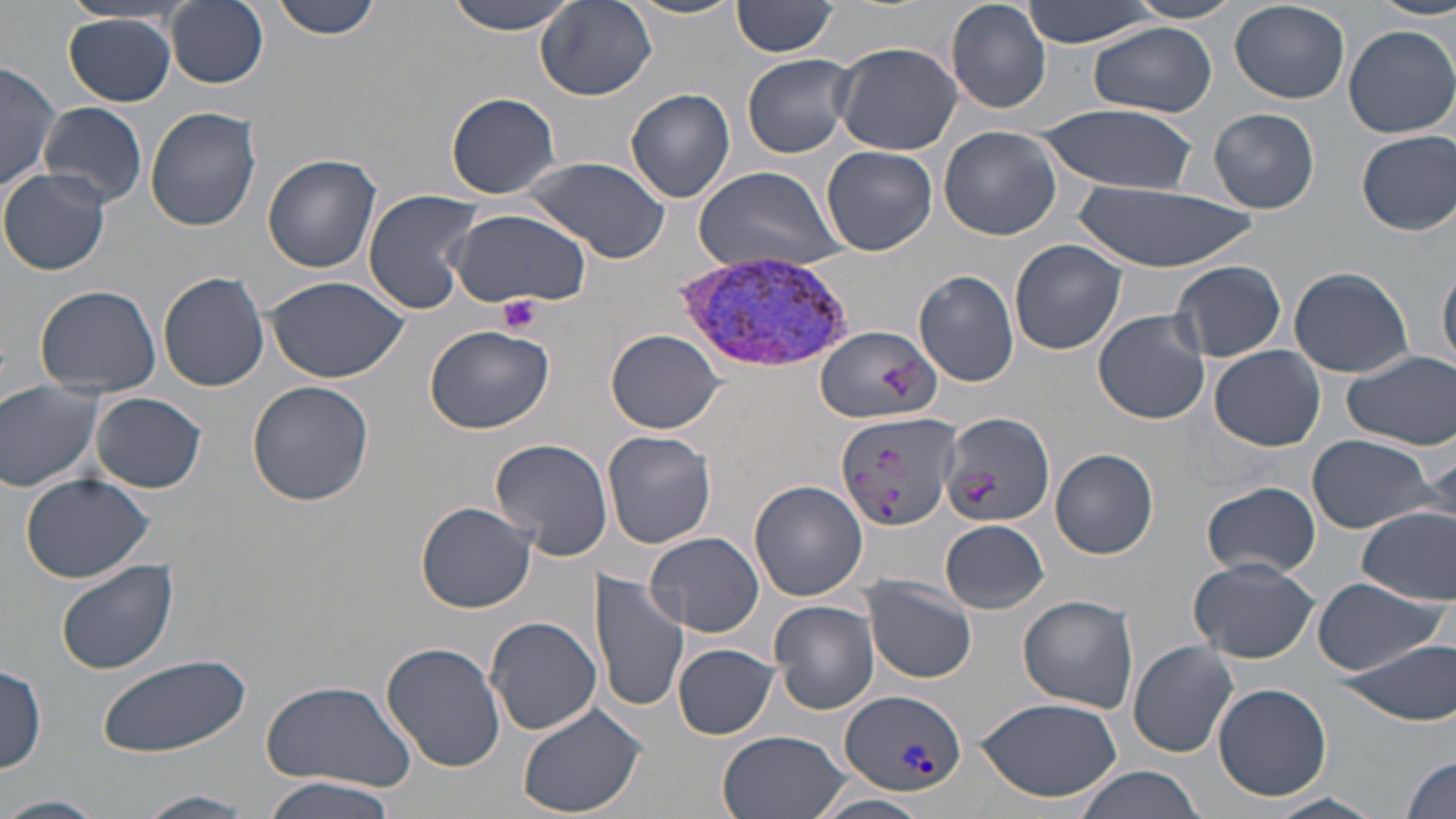

Summary:
  - Coordinate format: approximate bounding boxes as named x1/y1/x2/y2 corners in pixels
  - Platelet locations: (x1=500, y1=294, x2=540, y2=334)
  - Plasmodium vivax-infected red blood cell locations: (x1=677, y1=249, x2=853, y2=374), (x1=839, y1=689, x2=965, y2=797)
  - Uninfected red blood cell locations: (x1=165, y1=0, x2=270, y2=88), (x1=271, y1=0, x2=382, y2=40), (x1=442, y1=0, x2=584, y2=34), (x1=535, y1=0, x2=658, y2=101), (x1=624, y1=0, x2=747, y2=20), (x1=946, y1=0, x2=1052, y2=115), (x1=1019, y1=0, x2=1162, y2=48), (x1=1124, y1=0, x2=1246, y2=22), (x1=733, y1=1, x2=840, y2=57), (x1=1373, y1=1, x2=1456, y2=21), (x1=1229, y1=2, x2=1351, y2=104), (x1=65, y1=14, x2=179, y2=106), (x1=1087, y1=23, x2=1216, y2=117), (x1=1344, y1=25, x2=1456, y2=138), (x1=835, y1=40, x2=966, y2=156), (x1=742, y1=53, x2=856, y2=159), (x1=0, y1=59, x2=60, y2=192), (x1=626, y1=88, x2=736, y2=204), (x1=446, y1=92, x2=560, y2=198), (x1=39, y1=103, x2=147, y2=208), (x1=1034, y1=104, x2=1198, y2=193), (x1=146, y1=106, x2=261, y2=231), (x1=1210, y1=108, x2=1319, y2=214), (x1=939, y1=125, x2=1063, y2=241), (x1=1357, y1=130, x2=1456, y2=235), (x1=821, y1=145, x2=938, y2=256), (x1=263, y1=154, x2=381, y2=272), (x1=520, y1=155, x2=673, y2=265), (x1=688, y1=163, x2=849, y2=273), (x1=0, y1=170, x2=111, y2=275), (x1=1071, y1=183, x2=1257, y2=271), (x1=362, y1=189, x2=482, y2=315), (x1=446, y1=205, x2=591, y2=309), (x1=1009, y1=240, x2=1127, y2=355), (x1=1172, y1=260, x2=1287, y2=361), (x1=1439, y1=264, x2=1456, y2=372), (x1=1289, y1=266, x2=1413, y2=378), (x1=913, y1=270, x2=1021, y2=387), (x1=157, y1=271, x2=269, y2=392), (x1=268, y1=275, x2=407, y2=382), (x1=34, y1=284, x2=162, y2=397), (x1=1093, y1=309, x2=1212, y2=424), (x1=424, y1=324, x2=554, y2=434), (x1=816, y1=327, x2=941, y2=428), (x1=607, y1=329, x2=725, y2=432), (x1=1210, y1=346, x2=1324, y2=451), (x1=1340, y1=351, x2=1456, y2=449), (x1=0, y1=380, x2=105, y2=491), (x1=247, y1=381, x2=373, y2=506), (x1=90, y1=391, x2=206, y2=493), (x1=834, y1=409, x2=959, y2=533), (x1=940, y1=411, x2=1056, y2=532), (x1=602, y1=431, x2=718, y2=549), (x1=1306, y1=434, x2=1440, y2=534), (x1=489, y1=439, x2=615, y2=561), (x1=1332, y1=445, x2=1452, y2=594), (x1=1050, y1=448, x2=1159, y2=559), (x1=20, y1=473, x2=154, y2=583), (x1=749, y1=481, x2=868, y2=603), (x1=1204, y1=482, x2=1320, y2=577), (x1=415, y1=501, x2=537, y2=613), (x1=1355, y1=507, x2=1456, y2=605), (x1=942, y1=520, x2=1049, y2=613), (x1=644, y1=530, x2=765, y2=637), (x1=1189, y1=558, x2=1317, y2=663), (x1=56, y1=559, x2=178, y2=675), (x1=591, y1=570, x2=689, y2=713), (x1=864, y1=576, x2=978, y2=685), (x1=1313, y1=577, x2=1445, y2=676), (x1=1019, y1=594, x2=1138, y2=715), (x1=769, y1=599, x2=879, y2=715), (x1=486, y1=617, x2=602, y2=736), (x1=1338, y1=636, x2=1456, y2=725), (x1=381, y1=641, x2=506, y2=772), (x1=1128, y1=641, x2=1238, y2=758), (x1=673, y1=643, x2=779, y2=739), (x1=99, y1=653, x2=253, y2=759), (x1=0, y1=662, x2=48, y2=774), (x1=257, y1=679, x2=419, y2=791), (x1=1212, y1=682, x2=1331, y2=802), (x1=974, y1=697, x2=1122, y2=802), (x1=518, y1=702, x2=647, y2=818), (x1=718, y1=731, x2=847, y2=819), (x1=1400, y1=756, x2=1454, y2=819), (x1=1074, y1=767, x2=1207, y2=819), (x1=263, y1=777, x2=403, y2=819), (x1=140, y1=791, x2=254, y2=817), (x1=0, y1=794, x2=104, y2=819), (x1=1268, y1=794, x2=1383, y2=819), (x1=816, y1=796, x2=932, y2=819)
  - Slide-level diagnosis: Plasmodium vivax
  - Field of view: single
  - Magnification: 1000x
  - Stain: May-Grünwald-Giemsa
  - Image size: 1456×819 pixels
  - Modality: optical microscopy
  - Preparation: thin blood film